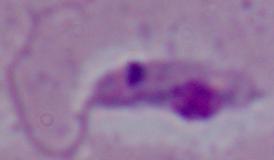
Summary:
  - Modality: photomicrograph
  - Magnification: 1000x
  - Identification: Leishmania